State the preparation type.
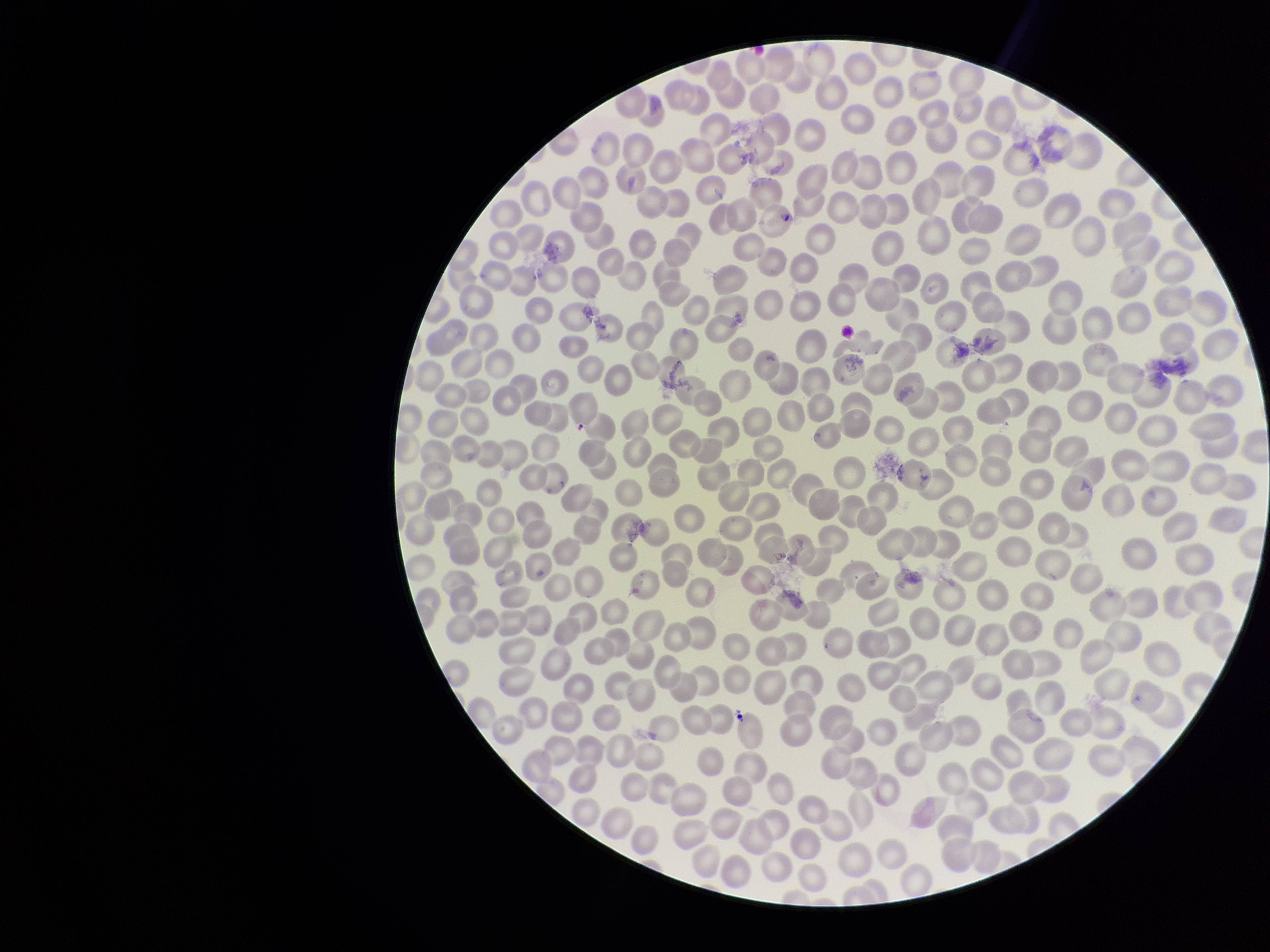
It is a thin blood smear.

Summary:
  - Parasitized red blood cells: none seen
  - Stain: Giemsa
  - Image size: 1270×952 pixels
  - Parasitized red blood cell count: 0
  - Capture: smartphone photograph through the microscope eyepiece
  - Patient malaria status: negative
  - Field of view: one from this slide
  - Red blood cell count: 344